Classify this cell by malaria status.
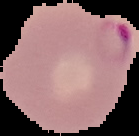

It is parasitized.

Summary:
  - Image type: segmented cell region on a black background
  - Image size: 139×136 pixels
  - Preparation: thin blood smear